Name the cell type shown.
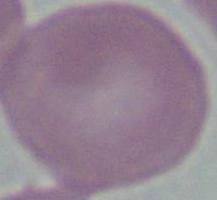

An erythrocyte.

modality = micrograph
magnification = 1000x